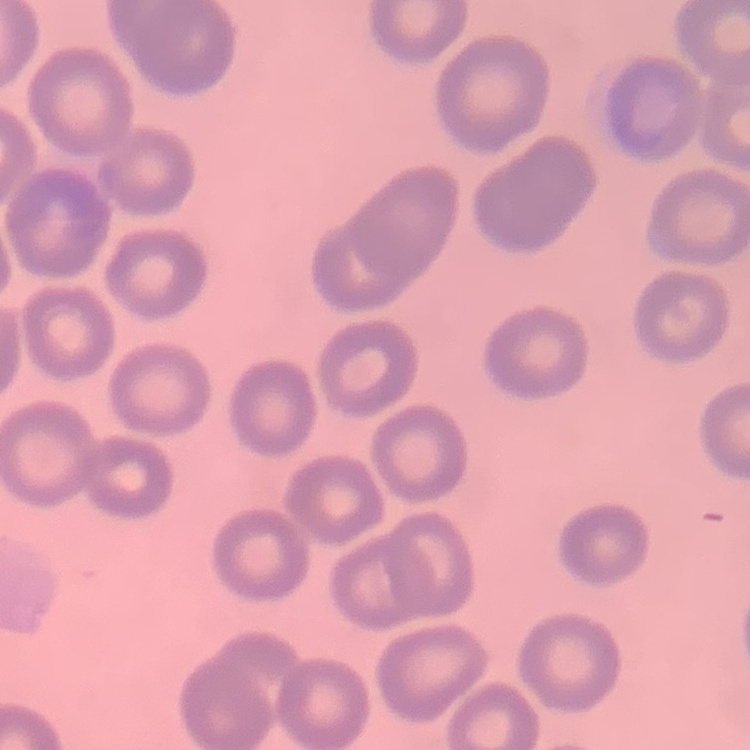

erythrocyte morphology = no rouleaux formation
image type = square crop of a larger photomicrograph
preparation = thin peripheral smear
stain = Field's or Giemsa